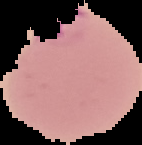

From a thin blood film. Result: malaria parasites detected. Image is 142×145 pixels. The area outside the segmented cell region is set to black.